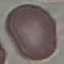 Malaria status: uninfected. Photographed with a smartphone camera at the microscope eyepiece. Thin blood smear. Giemsa-stained preparation. Automatically extracted cell patch, resized to 64 × 64 pixels.